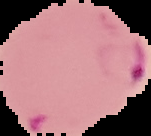

From a thin blood film. The area outside the segmented cell region is set to black. Malaria status: parasitized. Image is 151×136 pixels.